Name the blood parasite species.
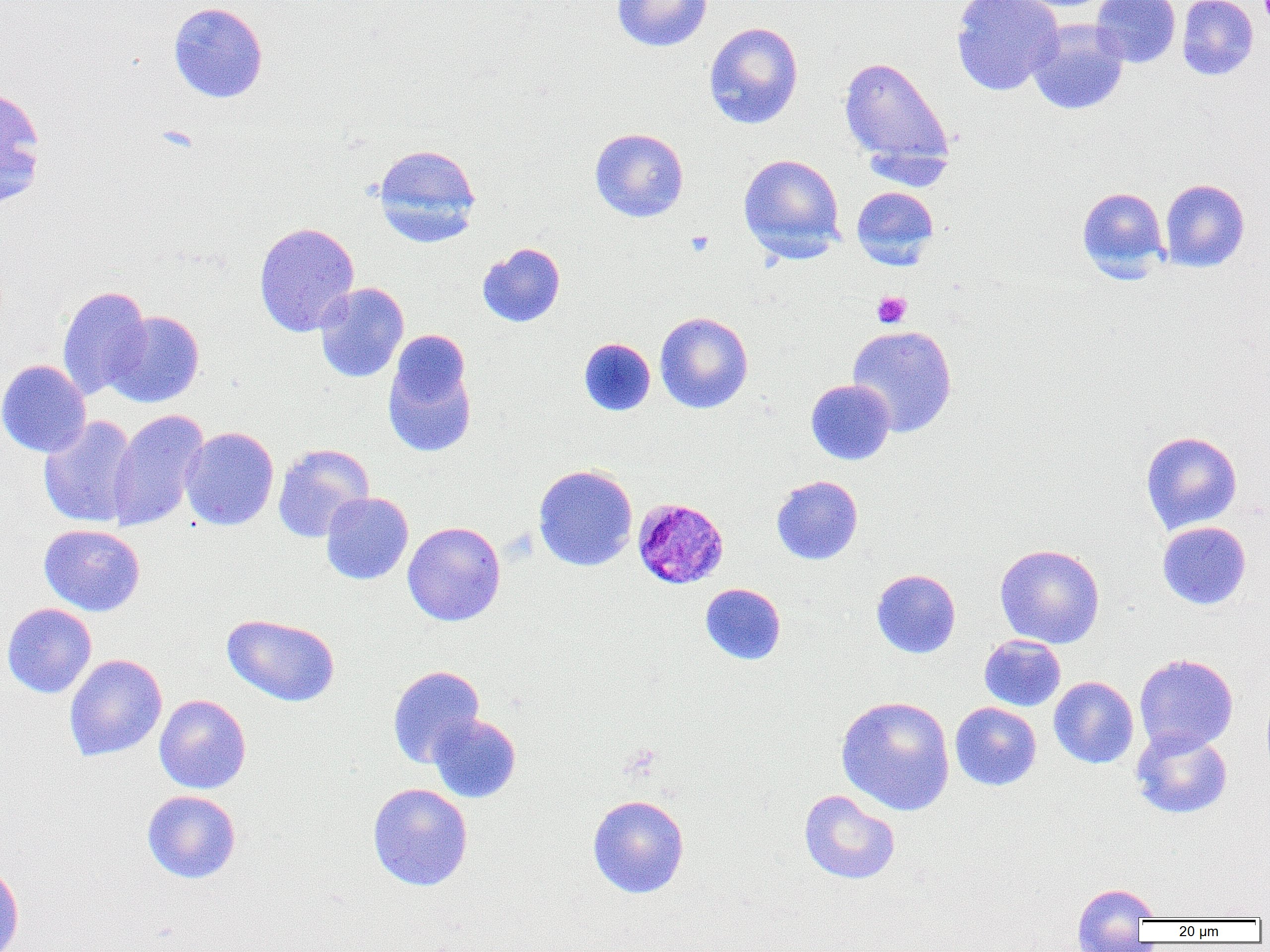
Plasmodium malariae.

Summary:
  - Coordinate format: approximate bounding boxes as [x1, y1, x2, y2] in pixels
  - Uninfected red blood cell locations: [612, 0, 713, 52], [950, 0, 1064, 96], [1091, 0, 1181, 68], [1177, 0, 1259, 80], [168, 2, 268, 104], [1027, 18, 1129, 115], [703, 21, 804, 129], [838, 55, 955, 177], [0, 87, 46, 206], [589, 127, 689, 222], [373, 143, 482, 247], [739, 154, 845, 261], [1160, 179, 1250, 272], [851, 185, 939, 268], [1076, 187, 1169, 280], [253, 221, 360, 338], [477, 242, 566, 328], [315, 283, 409, 383], [56, 285, 151, 400], [103, 310, 205, 408], [655, 312, 754, 414], [846, 324, 958, 437], [382, 336, 477, 459], [578, 337, 656, 416], [0, 359, 91, 458], [806, 379, 895, 465], [107, 409, 209, 532], [38, 415, 139, 528], [180, 426, 279, 531], [1141, 431, 1242, 534], [272, 443, 374, 543], [533, 464, 638, 571], [771, 475, 863, 565], [321, 492, 413, 585], [402, 521, 506, 626], [1157, 521, 1251, 610], [39, 523, 145, 616], [994, 543, 1105, 648], [871, 569, 961, 659], [700, 583, 786, 665], [1, 602, 97, 698], [222, 613, 341, 707], [979, 634, 1066, 711], [64, 654, 168, 761], [1134, 654, 1238, 754], [387, 665, 485, 768], [1049, 676, 1139, 769], [154, 694, 251, 794], [835, 695, 955, 816], [950, 702, 1041, 791], [427, 713, 522, 803], [1131, 727, 1232, 819], [367, 783, 473, 891], [798, 789, 901, 885], [142, 790, 241, 884], [587, 794, 689, 898], [0, 860, 24, 952], [1072, 882, 1159, 941]
  - Plasmodium malariae-infected red blood cell locations: [633, 497, 729, 589]
  - Platelet locations: [685, 231, 714, 256], [872, 291, 912, 329]
  - Magnification: 1000x
  - Image size: 1270×952 pixels
  - Field of view: one of a larger specimen
  - Modality: optical microscopy
  - Preparation: thin blood smear